State which parasite is depicted.
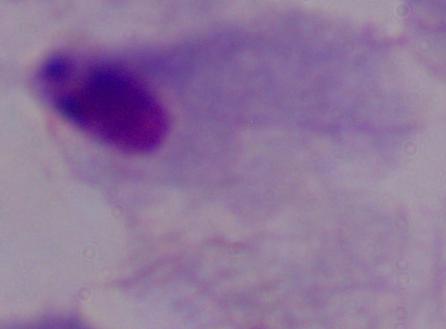

This is a trichomonad.

modality = photomicrograph
magnification = 1000x